Report the malaria status of this cell.
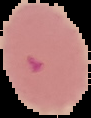
It is parasitized.

The area outside the segmented cell region is set to black. From a thin blood smear. Image is 91×118 pixels.